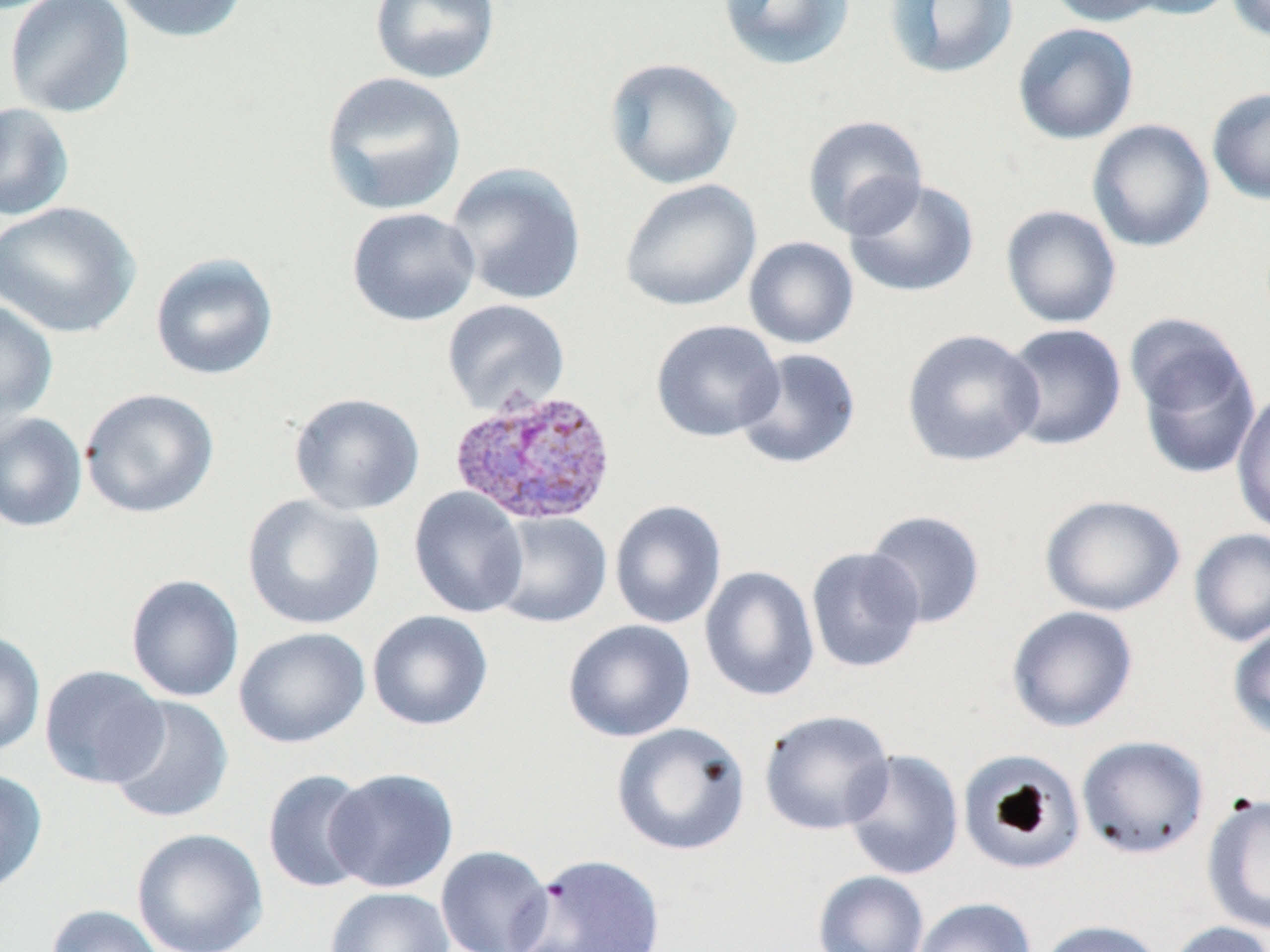

slide_level_diagnosis: Plasmodium vivax
uninfected_red_blood_cell_locations: 'approximate bounding boxes as (x1,y1)-(x2,y2) corner pairs in pixels: (4,0)-(136,119), (109,0)-(250,44), (368,0)-(501,85), (717,0)-(856,71), (883,0)-(1020,80), (1046,0)-(1166,26), (1121,0)-(1240,20), (1226,0)-(1270,43), (1012,23)-(1139,145), (603,57)-(742,190), (320,71)-(467,217), (1207,87)-(1270,205), (0,102)-(76,222), (802,114)-(928,239), (1086,119)-(1215,253), (444,162)-(587,306), (843,177)-(980,298), (619,178)-(762,312), (0,201)-(142,339), (1000,204)-(1122,329), (347,207)-(481,327), (743,236)-(859,349), (149,251)-(279,381), (442,299)-(570,415), (0,300)-(59,430), (650,319)-(785,443), (1001,323)-(1127,452), (900,328)-(1044,468), (1130,331)-(1263,480), (733,348)-(862,470), (79,388)-(219,518), (1231,388)-(1270,536), (288,393)-(425,516), (0,412)-(87,532), (408,487)-(529,619), (242,493)-(385,631), (1039,494)-(1186,617), (609,500)-(727,630), (863,509)-(987,629), (489,512)-(612,628), (1188,528)-(1270,647), (805,546)-(926,674), (699,565)-(820,702), (125,574)-(245,703), (1006,605)-(1139,733), (367,610)-(494,731), (562,619)-(696,742), (1227,620)-(1270,743), (233,627)-(371,749), (0,630)-(46,757), (39,664)-(169,789), (106,696)-(234,824), (759,709)-(895,836), (611,722)-(751,856), (1076,735)-(1209,860), (842,748)-(964,881), (957,749)-(1087,875), (325,767)-(459,893), (0,768)-(48,896), (262,769)-(375,894), (1201,793)-(1270,935), (131,828)-(268,952), (435,845)-(555,952), (513,852)-(667,952), (812,870)-(929,952), (325,887)-(455,952), (912,897)-(1036,952), (46,904)-(167,952), (1036,920)-(1167,952), (1165,921)-(1269,952)'
preparation: thin blood film
image_size: 1270×952 pixels
field_of_view: single
modality: optical microscopy
stain: May-Grünwald-Giemsa
magnification: 1000x
plasmodium_vivax_infected_red_blood_cell_locations: 'approximate bounding boxes as (x1,y1)-(x2,y2) corner pairs in pixels: (448,387)-(618,527)'